Outline each Plasmodium ovale-infected red blood cell.
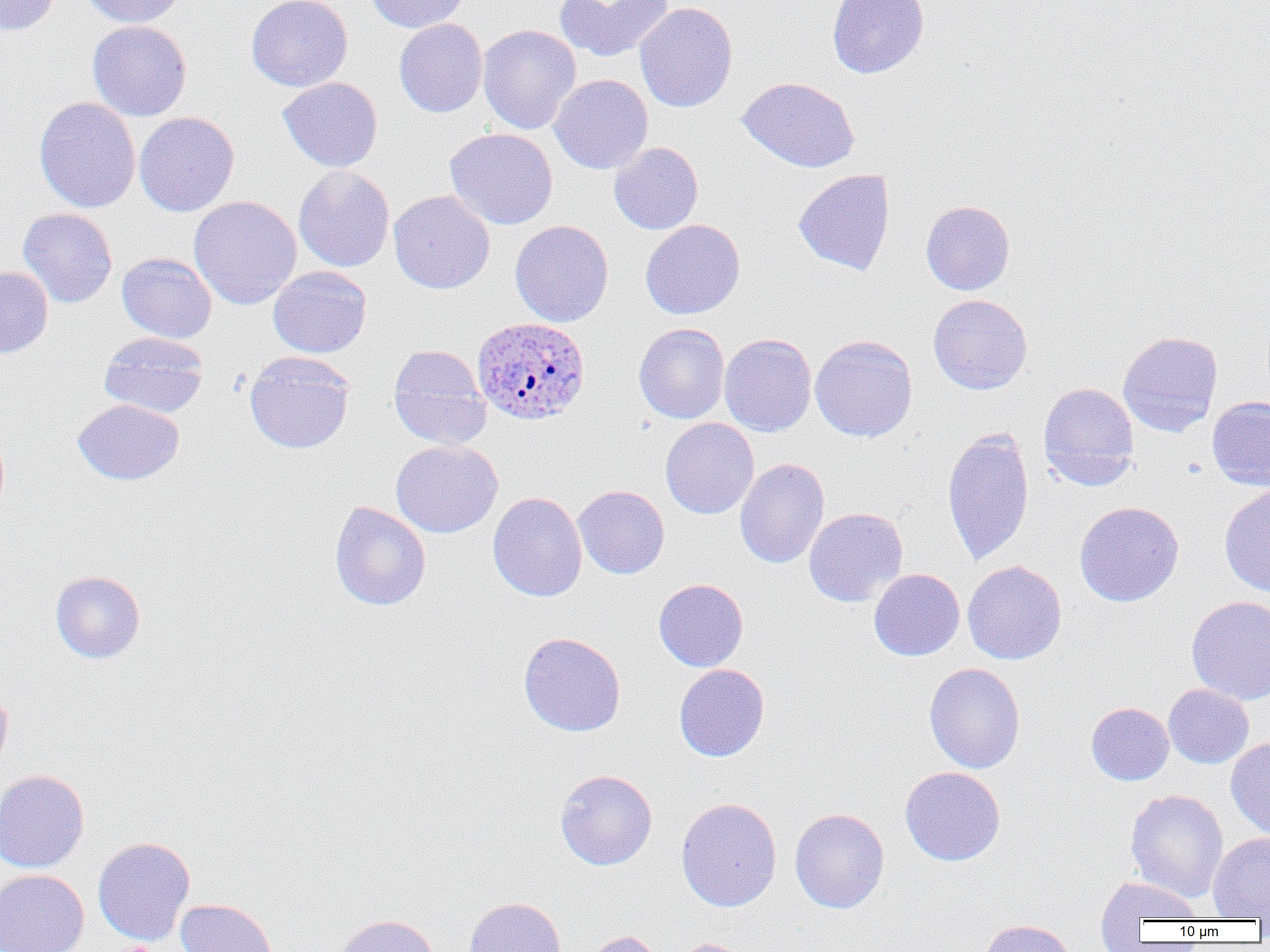
Approximate bounding boxes as (x1,y1)-(x2,y2) corner pairs in pixels.
Plasmodium ovale-infected red blood cells: (472,317)-(591,425).

slide-level diagnosis = Plasmodium ovale
uninfected red blood cell locations = approximate bounding boxes as (x1,y1)-(x2,y2) corner pairs in pixels: (0,0)-(60,35), (82,0)-(188,27), (246,0)-(353,92), (365,0)-(469,33), (555,0)-(672,62), (827,0)-(929,79), (635,2)-(738,112), (394,18)-(487,118), (87,20)-(192,121), (477,24)-(581,135), (549,74)-(653,174), (278,77)-(383,172), (738,77)-(860,172), (34,97)-(140,213), (134,112)-(239,217), (445,127)-(558,230), (609,142)-(703,234), (293,165)-(395,272), (793,168)-(895,276), (389,190)-(496,294), (188,195)-(301,310), (921,200)-(1015,295), (18,208)-(118,308), (640,219)-(745,319), (510,220)-(614,327), (117,252)-(217,343), (268,265)-(372,358), (0,266)-(53,359), (928,294)-(1033,395), (634,323)-(729,423), (1117,330)-(1223,437), (99,331)-(209,418), (719,333)-(817,437), (810,334)-(918,442), (388,345)-(491,449), (244,351)-(355,454), (1038,382)-(1139,490), (1207,396)-(1270,491), (72,399)-(184,486), (660,417)-(759,520), (942,428)-(1035,566), (391,440)-(503,538), (734,458)-(830,568), (1218,484)-(1270,597), (573,485)-(670,579), (487,491)-(587,602), (330,501)-(431,611), (1074,501)-(1184,607), (804,507)-(908,607), (963,560)-(1067,664), (869,568)-(965,661), (50,570)-(145,663), (653,578)-(749,672), (1186,595)-(1270,704), (518,631)-(626,737), (924,662)-(1026,773), (674,664)-(770,762), (1163,684)-(1254,769), (0,686)-(12,779), (1086,701)-(1174,785), (1226,737)-(1270,840), (900,766)-(1006,866), (0,769)-(89,873), (555,769)-(657,870), (1125,789)-(1228,902), (676,798)-(782,912), (789,808)-(889,913), (1208,832)-(1270,919), (92,836)-(195,945), (0,870)-(89,952), (1094,874)-(1204,929), (463,896)-(566,952), (175,898)-(278,952), (334,913)-(440,952), (980,919)-(1078,952), (580,929)-(666,952), (670,938)-(753,952)
preparation = thin blood film
field of view = one of a larger specimen
modality = light microscopy
image size = 1270×952 pixels
magnification = 1000x